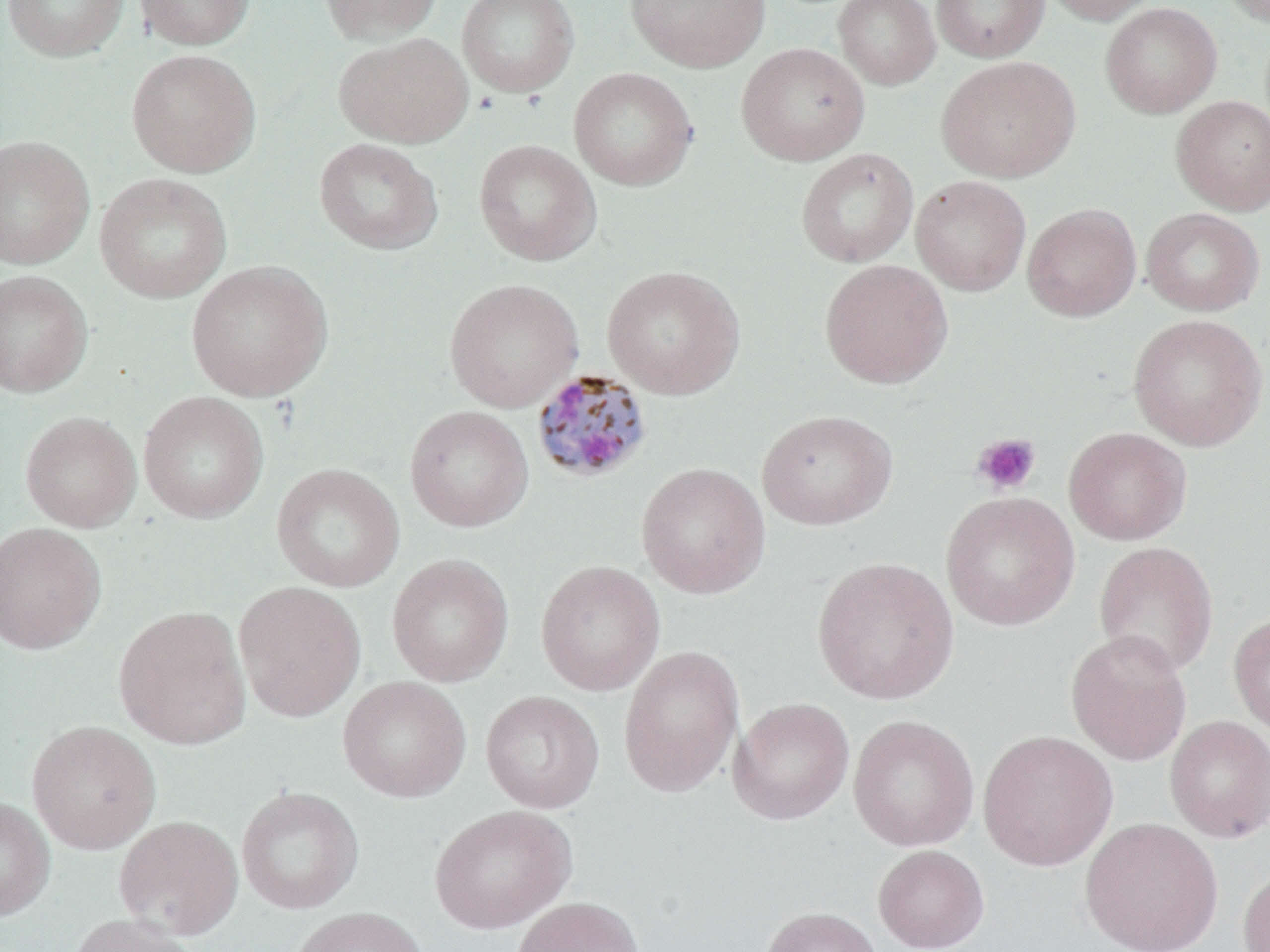

Summary:
  - Coordinate format: approximate bounding boxes as [x1, y1, x2, y2] in pixels
  - Plasmodium malariae-infected red blood cell locations: [530, 368, 653, 484]
  - Platelet locations: [971, 432, 1041, 496]
  - Uninfected red blood cell locations: [2, 0, 129, 61], [134, 0, 255, 51], [318, 0, 443, 44], [457, 0, 580, 97], [624, 0, 771, 73], [833, 0, 940, 90], [931, 0, 1050, 62], [1040, 0, 1163, 25], [1219, 0, 1270, 26], [1100, 2, 1222, 119], [334, 32, 473, 148], [736, 42, 870, 166], [126, 49, 261, 178], [936, 56, 1080, 183], [568, 67, 698, 190], [1171, 95, 1270, 215], [0, 135, 94, 270], [314, 138, 443, 255], [474, 139, 601, 266], [795, 147, 919, 268], [95, 173, 232, 304], [910, 175, 1031, 297], [1022, 203, 1141, 322], [1141, 208, 1265, 316], [819, 259, 953, 388], [186, 260, 333, 401], [602, 265, 745, 399], [0, 270, 93, 397], [443, 278, 583, 412], [1127, 314, 1268, 451], [138, 391, 269, 523], [404, 405, 534, 532], [757, 409, 898, 530], [20, 411, 142, 532], [1064, 426, 1191, 545], [636, 462, 770, 599], [271, 463, 405, 592], [941, 491, 1080, 631], [0, 522, 107, 654], [1093, 541, 1219, 678], [387, 553, 514, 687], [812, 555, 960, 705], [535, 560, 665, 696], [233, 581, 367, 723], [112, 605, 252, 750], [1228, 611, 1270, 737], [1065, 629, 1192, 766], [619, 644, 745, 797], [337, 676, 472, 802], [480, 690, 605, 813], [728, 697, 855, 825], [849, 715, 979, 851], [1164, 715, 1270, 842], [26, 720, 161, 854], [978, 729, 1118, 871], [236, 786, 365, 914], [0, 796, 55, 921], [429, 804, 576, 934], [113, 815, 244, 941], [1079, 817, 1223, 952], [873, 844, 990, 952], [1237, 865, 1270, 951], [510, 896, 646, 952], [760, 906, 884, 952], [289, 907, 429, 952], [65, 913, 202, 952]
  - Slide-level diagnosis: Plasmodium malariae
  - Stain: May-Grünwald-Giemsa
  - Field of view: one of a larger specimen
  - Preparation: thin blood film
  - Modality: optical microscopy
  - Magnification: 1000x
  - Image size: 1270×952 pixels